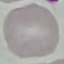
Malaria status: uninfected. Giemsa stain. Cell patch, automatically extracted from a larger field of view and resized to 64 × 64 pixels. Thin blood film. Acquired by smartphone through the microscope eyepiece.